Comment on the morphology of the erythrocytes.
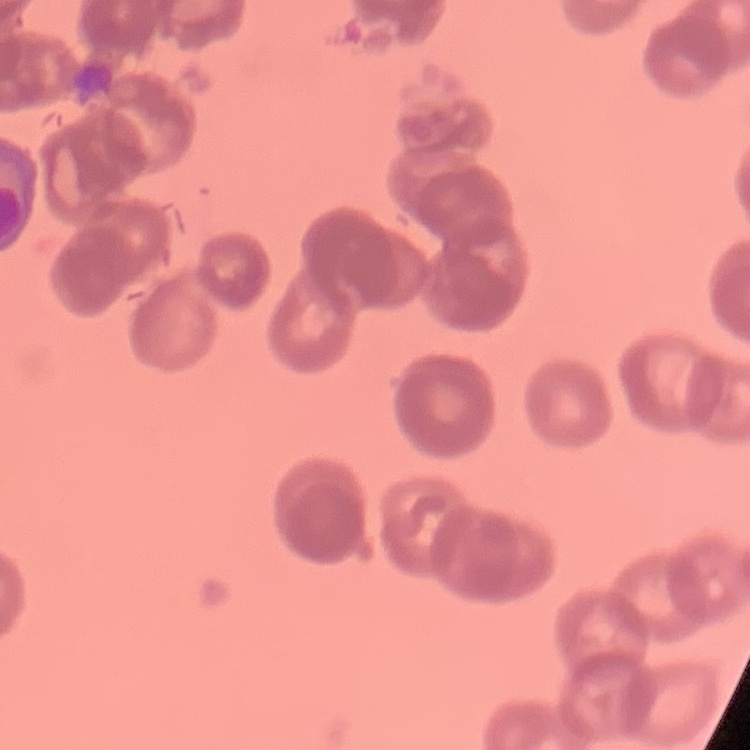
They show rouleaux formation.

preparation = thin blood smear
stain = Field's or Giemsa
image type = one tile cut from a larger photomicrograph